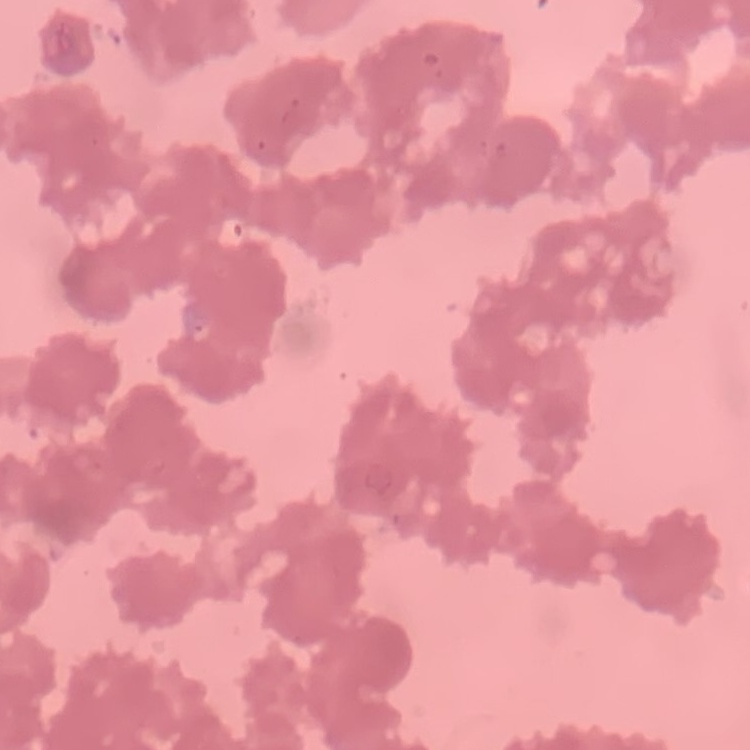
The red blood cells show rouleaux formation. Square crop of a larger photomicrograph. Thin blood film. Field's or Giemsa stain.